Locate every malaria parasite and every leukocyte.
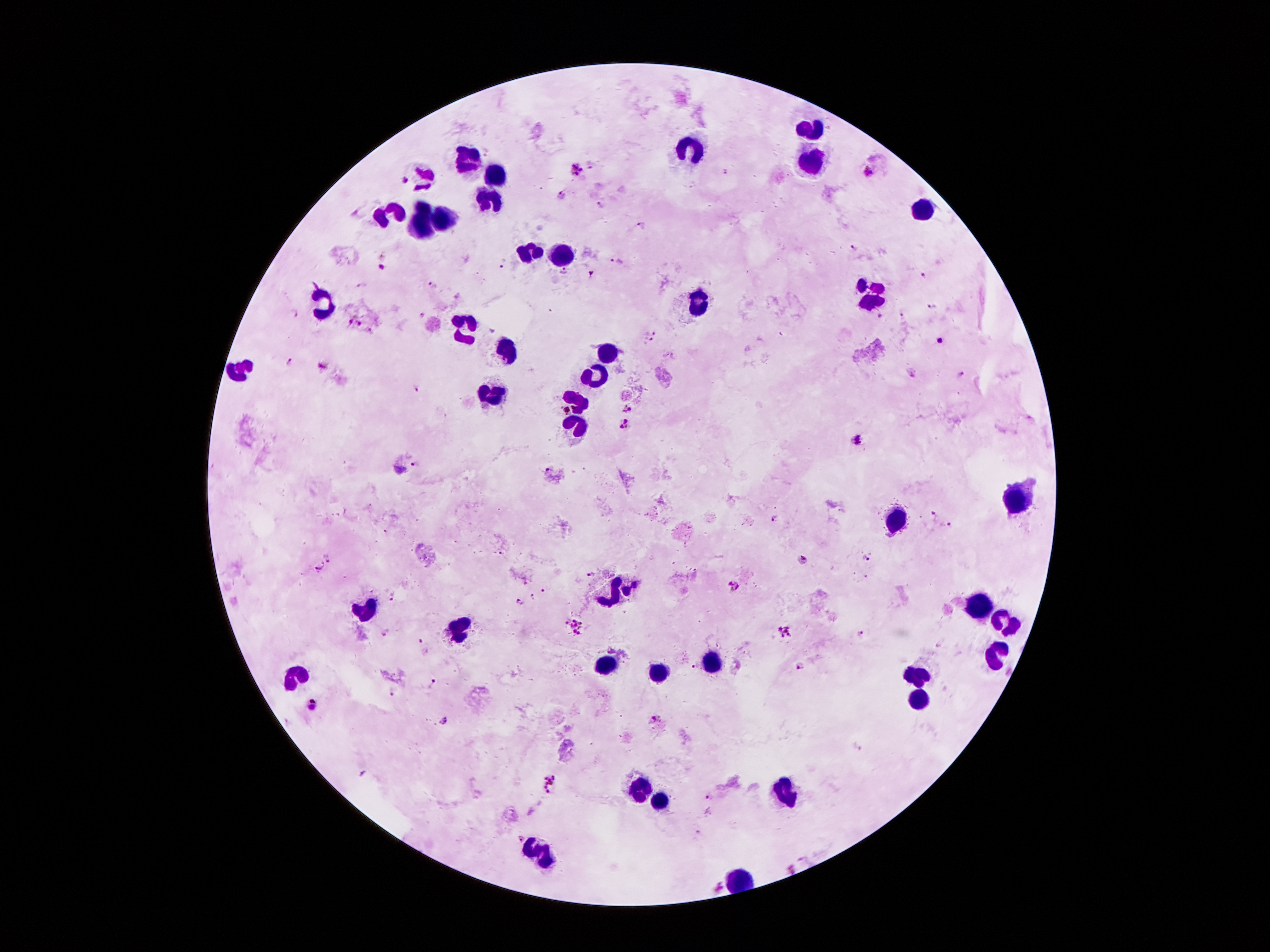
Approximate object centers, in pixels from the top-left corner.
Malaria parasites: (x=589, y=164), (x=575, y=171), (x=868, y=172), (x=405, y=178), (x=564, y=195), (x=643, y=225), (x=851, y=248), (x=615, y=261), (x=501, y=263), (x=380, y=266), (x=565, y=272), (x=590, y=272), (x=923, y=276), (x=431, y=285), (x=361, y=286), (x=458, y=295), (x=933, y=305), (x=295, y=312), (x=420, y=313), (x=902, y=314), (x=880, y=318), (x=349, y=321), (x=361, y=324), (x=369, y=329), (x=653, y=331), (x=941, y=340), (x=647, y=342), (x=287, y=361), (x=322, y=366), (x=910, y=372), (x=962, y=374), (x=417, y=387), (x=625, y=408), (x=625, y=424), (x=858, y=439), (x=415, y=463), (x=548, y=469), (x=401, y=470), (x=932, y=514), (x=773, y=517), (x=951, y=524), (x=326, y=557), (x=868, y=557), (x=805, y=559), (x=320, y=569), (x=592, y=573), (x=526, y=580), (x=734, y=585), (x=544, y=590), (x=533, y=596), (x=392, y=597), (x=521, y=603), (x=573, y=626), (x=387, y=631), (x=786, y=632), (x=860, y=633), (x=422, y=641), (x=695, y=663), (x=801, y=665), (x=433, y=682), (x=393, y=691), (x=311, y=702), (x=654, y=718), (x=445, y=721), (x=859, y=748), (x=551, y=785), (x=708, y=798), (x=699, y=835), (x=519, y=838), (x=791, y=868), (x=720, y=887).
Leukocytes: (x=810, y=128), (x=695, y=147), (x=810, y=159), (x=470, y=163), (x=495, y=171), (x=425, y=175), (x=490, y=200), (x=425, y=208), (x=923, y=212), (x=390, y=214), (x=439, y=221), (x=421, y=223), (x=531, y=253), (x=560, y=253), (x=870, y=292), (x=327, y=300), (x=697, y=302), (x=464, y=325), (x=505, y=350), (x=603, y=350), (x=243, y=368), (x=597, y=372), (x=486, y=395), (x=577, y=405), (x=577, y=425), (x=1017, y=501), (x=898, y=522), (x=613, y=591), (x=976, y=606), (x=363, y=610), (x=1005, y=620), (x=458, y=626), (x=997, y=655), (x=710, y=661), (x=607, y=663), (x=290, y=675), (x=654, y=675), (x=917, y=675), (x=919, y=702), (x=634, y=792), (x=786, y=792), (x=659, y=804), (x=542, y=851).

Summary:
  - Image size: 1270×952 pixels
  - Preparation: thick peripheral-blood smear
  - Patient malaria status: positive for Plasmodium falciparum
  - Capture: smartphone through the microscope eyepiece
  - Magnification: 100x
  - Stain: Giemsa
  - Field of view: single